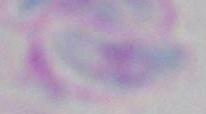

Summary:
  - Modality: photomicrograph
  - Magnification: 1000x
  - Identification: Toxoplasma gondii